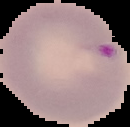
image size = 130×127 pixels
result = Plasmodium parasites identified
image type = cell region segmented out of the field of view; surrounding area masked to black
preparation = thin blood film